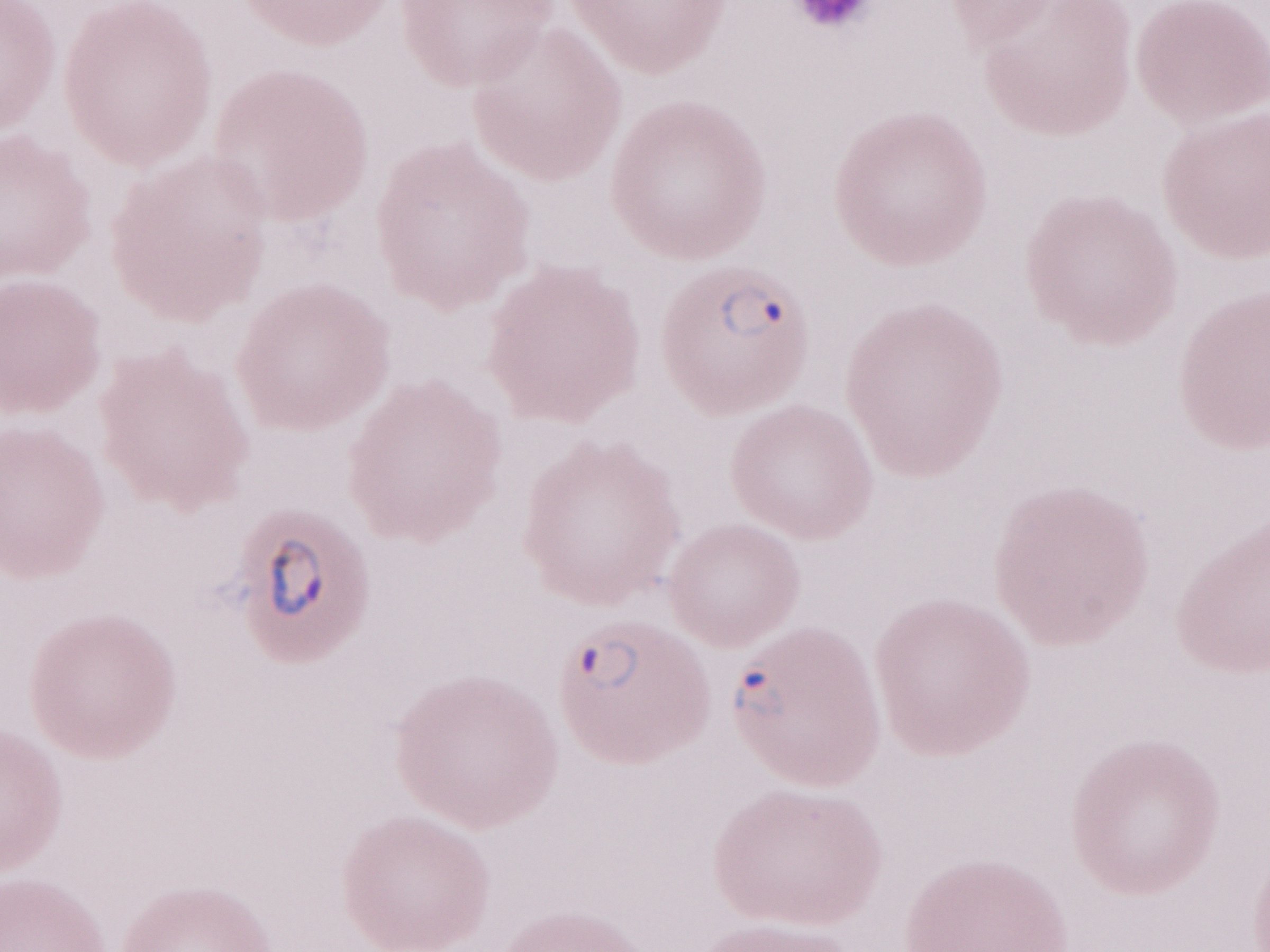 Patient diagnosis: malaria infection. Olympus BX43 microscope, Olympus DP73 camera. Image is 1270×952 pixels. 1,000x magnification. May-Grünwald-Giemsa stain. Thin blood film. One field of this slide.